Describe the morphology of the erythrocytes.
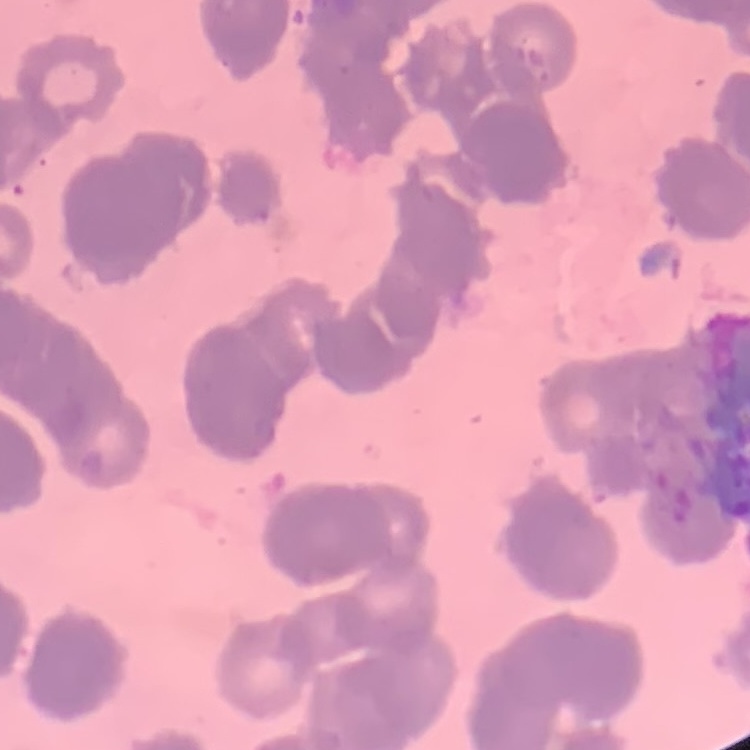
They show rouleaux formation.

Summary:
  - Preparation: thin blood smear
  - Image type: square crop of a larger photomicrograph
  - Stain: Field's or Giemsa